Classify this cell by malaria status.
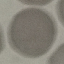
Uninfected.

Summary:
  - Preparation: thin smear
  - Stain: Giemsa
  - Capture: smartphone camera at the microscope eyepiece
  - Image type: cell patch, automatically extracted from a larger field of view and resized to 64 × 64 pixels